Identify the parasite.
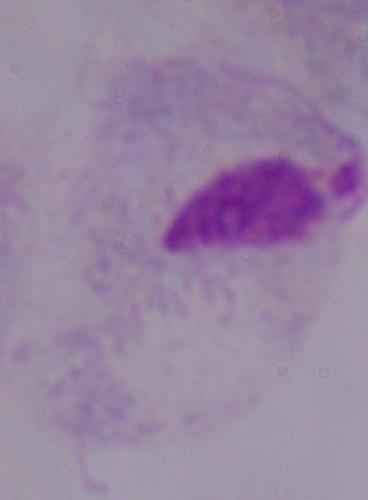
This is a trichomonad.

magnification = 1000x
modality = photomicrograph